Assess this cell for malaria.
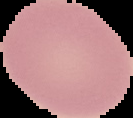

It is uninfected.

From a thin blood film. Image is 133×118 pixels. Segmented cell region on a black background.